Name the cell type shown.
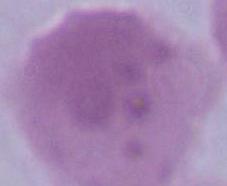
This is an erythrocyte.

Summary:
  - Modality: micrograph
  - Magnification: 1000x